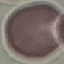
{
  "malaria_status": "uninfected",
  "stain": "Giemsa",
  "preparation": "thin blood smear",
  "capture": "smartphone camera at the microscope eyepiece",
  "image_type": "cell patch, automatically extracted from a larger field of view and resized to 64 × 64 pixels"
}